Report the malaria status of this cell.
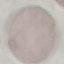

Uninfected.

{
  "preparation": "thin blood smear",
  "capture": "smartphone through the microscope eyepiece",
  "image_type": "cell patch, automatically extracted from a larger field of view and resized to 64 × 64 pixels",
  "stain": "Giemsa"
}